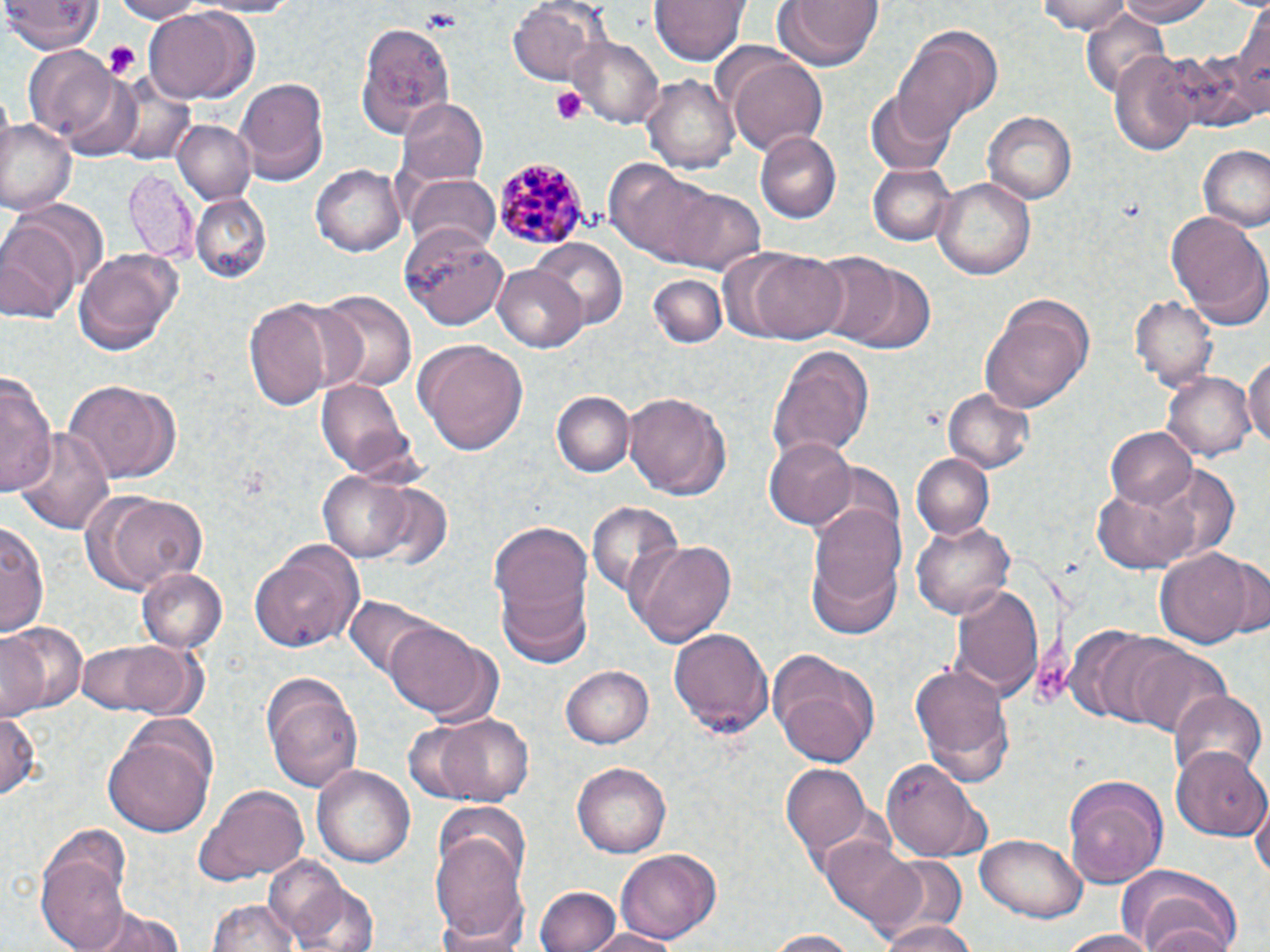
Summary:
  - Coordinate format: approximate bounding boxes as (x1, y1, x2, y2) in pixels
  - Plasmodium malariae-infected red blood cell locations: (494, 158, 589, 250)
  - Uninfected red blood cell locations: (104, 0, 204, 23), (187, 0, 308, 15), (508, 0, 605, 87), (651, 0, 753, 65), (770, 0, 886, 70), (1038, 0, 1134, 32), (1114, 0, 1221, 26), (5, 1, 103, 55), (143, 7, 247, 104), (1083, 11, 1174, 98), (356, 23, 454, 143), (891, 26, 1001, 131), (565, 34, 666, 129), (1183, 43, 1267, 134), (23, 47, 118, 139), (725, 49, 830, 157), (1110, 49, 1202, 157), (643, 73, 739, 176), (235, 75, 327, 178), (866, 90, 954, 174), (398, 97, 489, 185), (983, 112, 1077, 204), (0, 118, 76, 214), (173, 119, 256, 206), (755, 133, 841, 222), (1197, 145, 1270, 231), (609, 161, 767, 272), (311, 162, 406, 256), (868, 162, 955, 246), (124, 168, 196, 259), (932, 174, 1038, 279), (404, 175, 501, 255), (190, 193, 271, 283), (1164, 208, 1270, 331), (0, 220, 81, 324), (399, 223, 507, 330), (530, 237, 629, 331), (72, 246, 184, 357), (748, 250, 850, 343), (804, 251, 900, 346), (840, 261, 933, 351), (491, 263, 589, 351), (647, 274, 728, 349), (314, 290, 416, 394), (1131, 295, 1215, 389), (243, 296, 340, 411), (980, 296, 1095, 412), (414, 339, 530, 455), (767, 345, 876, 464), (1243, 354, 1270, 454), (1163, 370, 1255, 462), (0, 372, 55, 503), (315, 378, 411, 475), (60, 379, 173, 483), (939, 387, 1034, 474), (621, 389, 734, 500), (552, 391, 633, 477), (16, 424, 115, 534), (1104, 426, 1198, 510), (766, 434, 859, 529), (912, 454, 994, 539), (1154, 464, 1239, 563), (319, 469, 416, 562), (1089, 479, 1204, 574), (357, 482, 457, 574), (85, 490, 210, 593), (810, 499, 909, 606), (586, 503, 686, 601), (909, 515, 1016, 620), (1, 518, 47, 640), (489, 518, 596, 662), (250, 538, 367, 653), (628, 538, 735, 647), (1156, 549, 1256, 648), (805, 551, 903, 642), (1220, 553, 1269, 640), (138, 568, 227, 654), (953, 583, 1044, 699), (343, 595, 449, 688), (383, 620, 498, 724), (0, 622, 84, 721), (667, 623, 772, 736), (1071, 627, 1174, 725), (74, 637, 205, 719), (1116, 638, 1231, 739), (765, 649, 881, 768), (910, 658, 1012, 777), (560, 665, 654, 749), (261, 672, 362, 796), (1170, 690, 1264, 781), (0, 710, 41, 806), (407, 711, 537, 806), (103, 719, 218, 838), (1172, 748, 1269, 841), (881, 760, 988, 865), (781, 761, 875, 866), (572, 762, 672, 857), (312, 763, 416, 870), (1064, 774, 1169, 886), (196, 784, 310, 884), (1251, 795, 1269, 886), (434, 799, 533, 896), (428, 833, 532, 952), (817, 835, 933, 935), (976, 835, 1089, 922), (41, 846, 131, 952), (616, 847, 720, 946), (266, 856, 353, 944), (1114, 864, 1245, 952), (875, 871, 973, 952), (292, 880, 379, 952), (535, 886, 621, 952), (206, 899, 304, 952), (85, 905, 189, 952), (1134, 905, 1242, 952), (874, 916, 975, 952), (576, 926, 684, 952), (1058, 929, 1166, 952), (760, 930, 867, 951)
  - Platelet locations: (418, 8, 463, 32), (101, 41, 142, 78), (552, 86, 588, 125)
  - Slide-level diagnosis: Plasmodium malariae
  - Preparation: thin blood film
  - Magnification: 1000x
  - Field of view: one of a larger specimen
  - Modality: light microscopy
  - Image size: 1270×952 pixels
  - Stain: May-Grünwald-Giemsa